Classify this cell by malaria status.
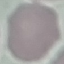

It is uninfected.

Summary:
  - Stain: Giemsa
  - Preparation: thin blood film
  - Capture: smartphone through the microscope eyepiece
  - Image type: automatically extracted cell patch, resized to 64 × 64 pixels